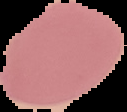

Image is 127×112 pixels. The area outside the segmented cell region is set to black. From a thin blood film. Result: negative for malaria parasites.